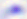
Summary:
  - Identification: Toxoplasma gondii
  - Modality: photomicrograph
  - Magnification: 400x